Comment on the morphology of the erythrocytes.
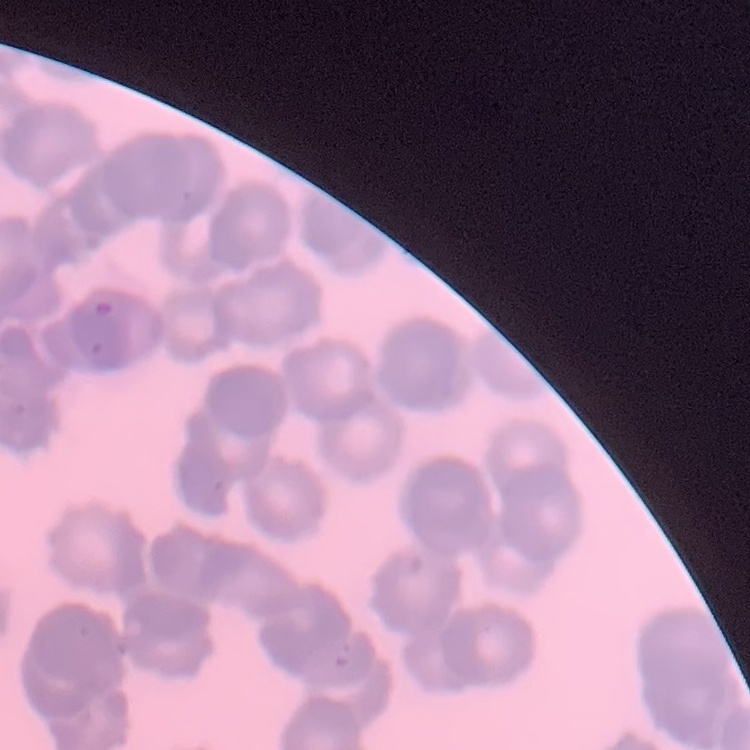

Rouleaux formation.

stain = Field's or Giemsa
image type = square crop of a larger photomicrograph
preparation = thin blood smear